Comment on the morphology of the red blood cells.
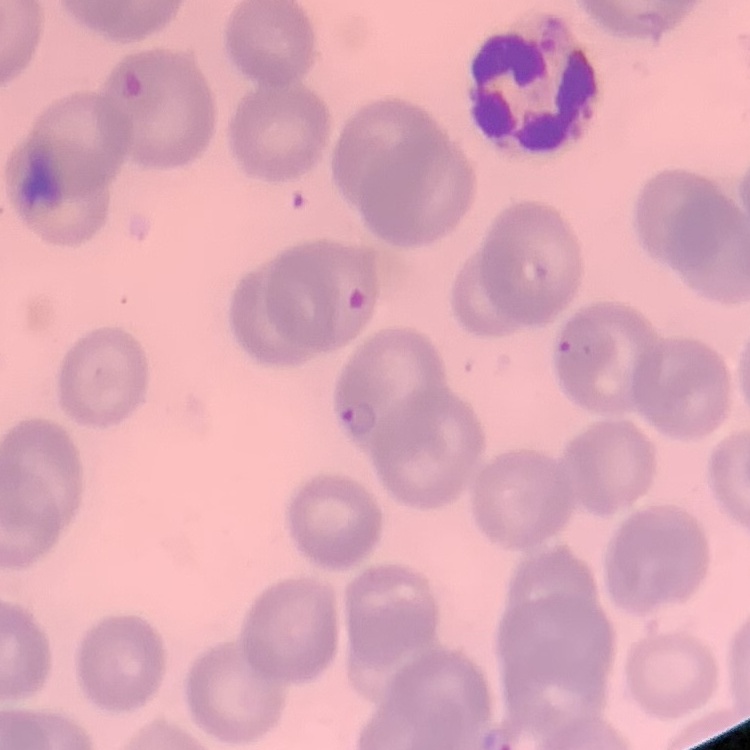
No rouleaux formation.

Summary:
  - Stain: Field's or Giemsa
  - Image type: one tile cut from a larger photomicrograph
  - Preparation: thin blood film